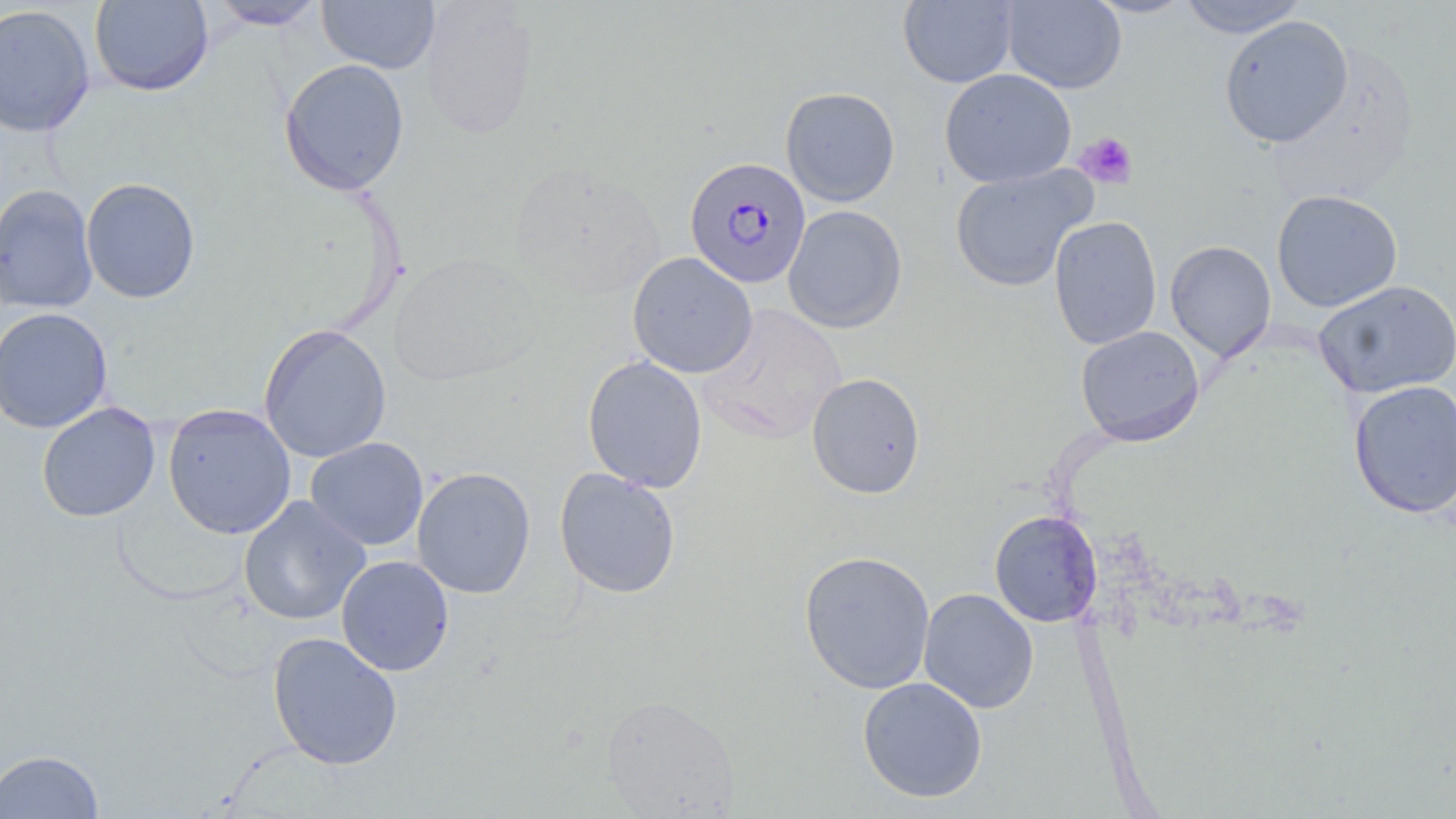
slide-level diagnosis = Plasmodium falciparum
uninfected red blood cell locations = approximate bounding boxes as (x1, y1, x2, y2) in pixels: (89, 0, 213, 96), (1084, 0, 1196, 18), (1177, 0, 1309, 38), (207, 1, 329, 30), (317, 1, 440, 74), (898, 1, 1018, 88), (1002, 1, 1126, 93), (419, 2, 539, 140), (0, 3, 96, 137), (1219, 15, 1354, 148), (279, 58, 410, 195), (939, 68, 1076, 188), (781, 86, 901, 206), (507, 163, 667, 302), (950, 163, 1096, 293), (81, 177, 201, 303), (0, 184, 99, 313), (1271, 189, 1403, 313), (782, 205, 907, 333), (1048, 216, 1162, 350), (1164, 239, 1277, 363), (627, 251, 757, 379), (389, 252, 544, 386), (1313, 280, 1456, 399), (697, 304, 847, 445), (0, 306, 112, 433), (258, 324, 391, 463), (1076, 325, 1205, 446), (582, 355, 707, 493), (806, 372, 926, 499), (1348, 378, 1456, 519), (37, 402, 160, 522), (163, 403, 296, 539), (305, 436, 429, 551), (411, 466, 536, 599), (554, 467, 681, 598), (239, 496, 371, 625), (989, 510, 1103, 627), (798, 549, 936, 695), (336, 555, 454, 676), (918, 588, 1038, 713), (267, 631, 403, 770), (857, 676, 988, 802), (601, 694, 740, 817), (1, 749, 104, 818)
field of view = single
modality = light microscopy
magnification = 1000x
Plasmodium falciparum-infected red blood cell locations = approximate bounding boxes as (x1, y1, x2, y2) in pixels: (684, 156, 812, 289)
preparation = thin blood smear
image size = 1456×819 pixels
platelet locations = approximate bounding boxes as (x1, y1, x2, y2) in pixels: (1075, 132, 1138, 190)
stain = May-Grünwald-Giemsa